Locate every Plasmodium falciparum parasite and identify its life-cycle stage.
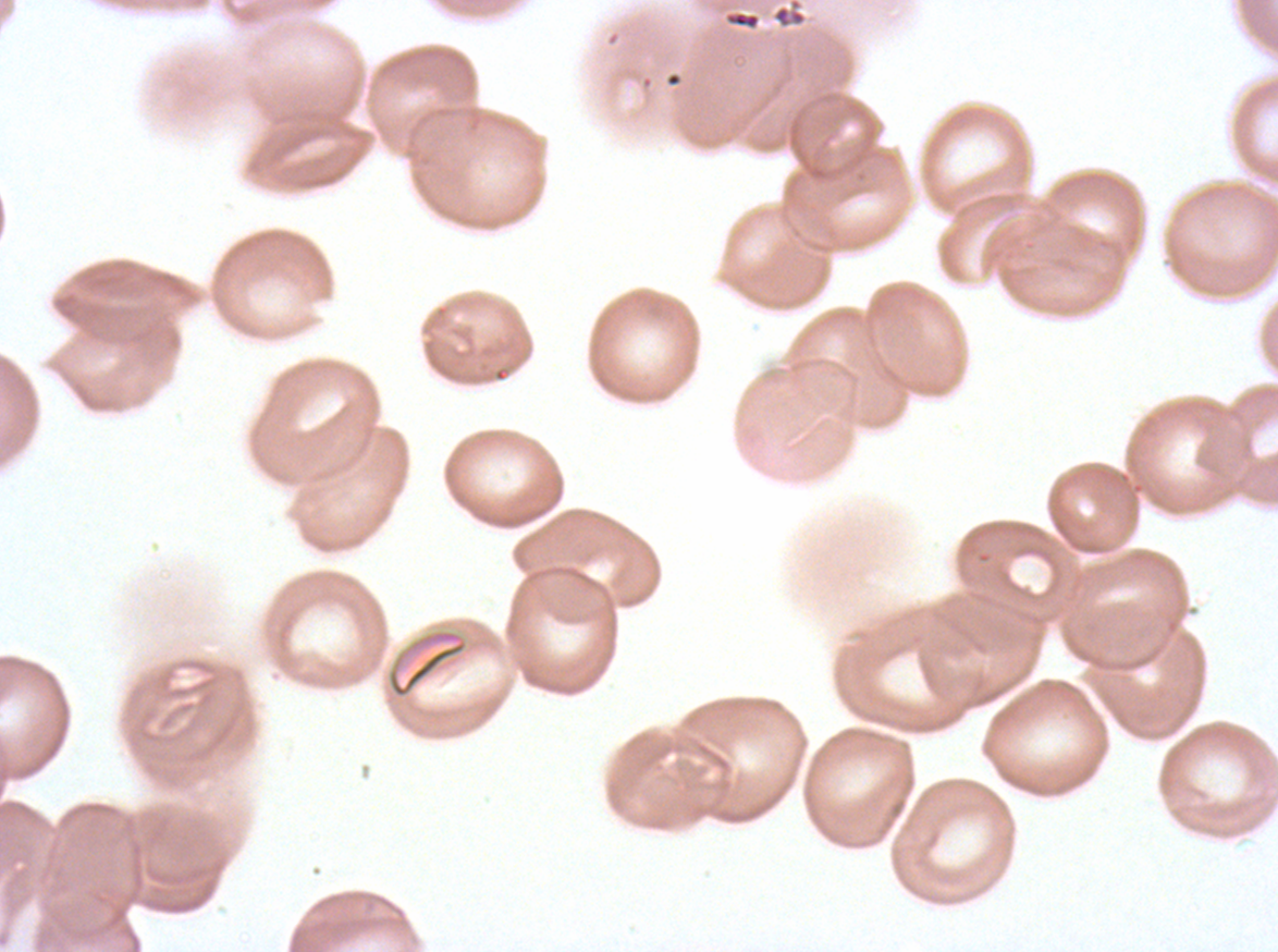

No rings, late-ring/early-trophozoite forms, mid trophozoites, late trophozoites, early schizonts, late schizonts, segmenters, or gametocytes observed.

Approximate bounding rectangles given as corner coordinates in pixels from the top-left. Debris locations: (x1=725, y1=10, x2=761, y2=30), (x1=387, y1=629, x2=469, y2=699). Image is 1278×952 pixels. Giemsa-stained preparation. Ex-vivo Plasmodium falciparum culture from a patient in The Gambia, grown for 24 to 48 hours. One sub-image of a larger composite. Thin blood smear.